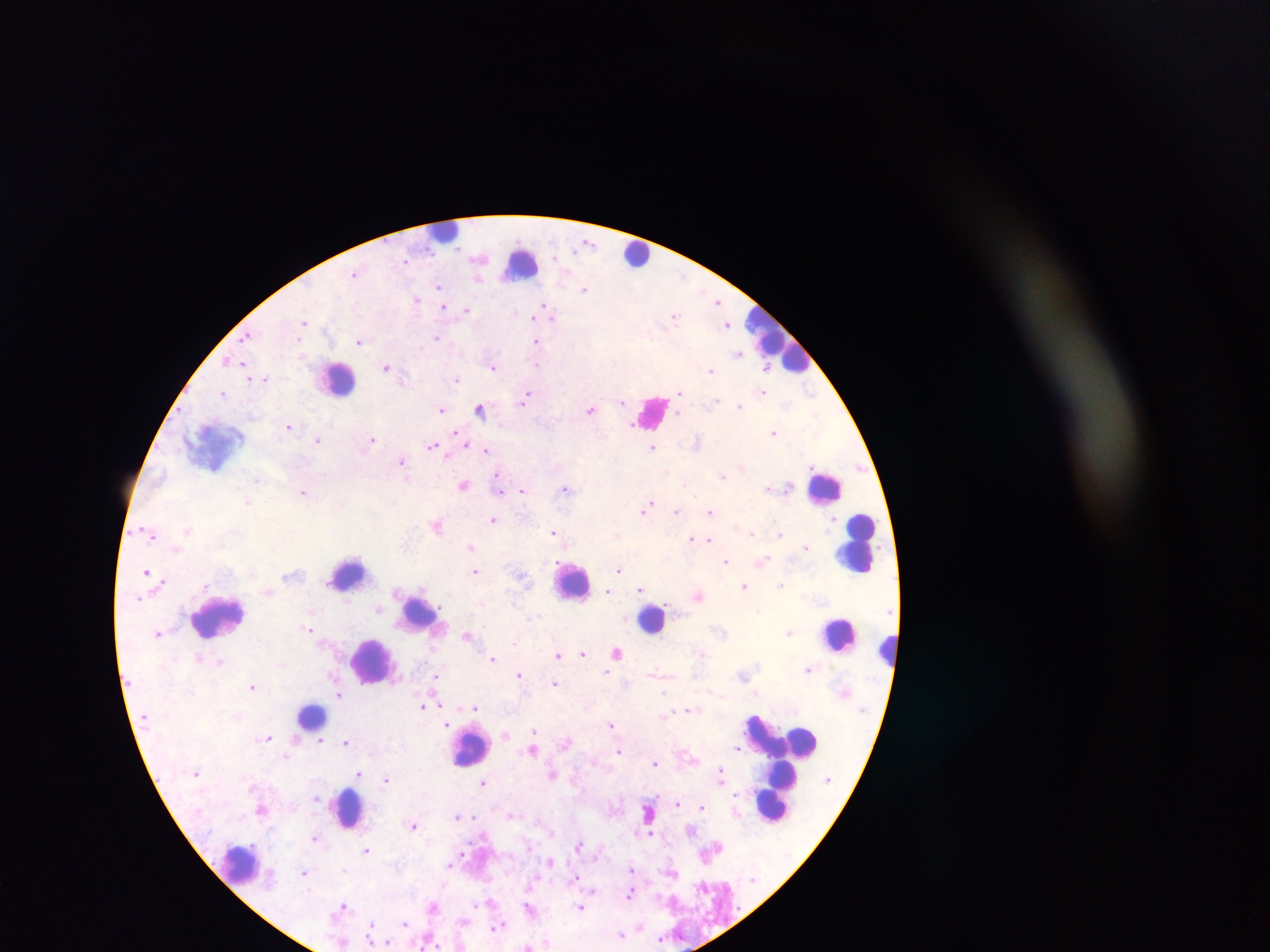

field of view = single
image size = 1270×952 pixels
leukocyte locations = approximate centers as [x, y] in pixels: [439, 233], [638, 256], [521, 260], [774, 343], [334, 378], [820, 486], [857, 547], [349, 573], [566, 584], [225, 610], [421, 611], [653, 618], [840, 636], [890, 648], [374, 662], [312, 719], [809, 737], [474, 743], [791, 773], [347, 806], [771, 806], [237, 862]
malaria parasite locations = approximate centers as [x, y] in pixels: [406, 257], [478, 258], [406, 259], [355, 273], [685, 274], [480, 278], [436, 289], [584, 289], [439, 291], [416, 298], [717, 302], [544, 306], [442, 307], [447, 308], [466, 310], [674, 314], [305, 320], [553, 320], [726, 324], [302, 326], [249, 335], [436, 338], [297, 342], [359, 342], [535, 342], [738, 354], [301, 356], [242, 362], [536, 366], [767, 366], [386, 367], [494, 368], [710, 369], [265, 376], [458, 379], [679, 390], [221, 392], [527, 392], [764, 392], [812, 393], [677, 395], [526, 397], [620, 401], [523, 403], [740, 406], [479, 407], [440, 408], [591, 410], [289, 425], [633, 426], [455, 431], [773, 432], [319, 439], [373, 440], [466, 443], [431, 446], [655, 449], [487, 450], [447, 459], [401, 462], [496, 473], [724, 476], [257, 480], [464, 486], [566, 488], [521, 490], [304, 492], [499, 493], [249, 503], [649, 503], [647, 509], [676, 511], [710, 512], [494, 519], [437, 526], [188, 530], [551, 532], [752, 533], [781, 533], [152, 535], [692, 538], [709, 539], [471, 547], [806, 547], [765, 560], [725, 562], [618, 570], [474, 571], [146, 573], [161, 582], [782, 584], [745, 587], [640, 591], [608, 592], [139, 600], [379, 609], [538, 616], [310, 629], [790, 632], [158, 633], [467, 637], [617, 652], [582, 654], [559, 655], [198, 658], [494, 658], [219, 662], [808, 669], [607, 672], [517, 674], [435, 675], [332, 676], [554, 683], [252, 687], [335, 689], [665, 692], [339, 694], [442, 707], [423, 708], [474, 708], [691, 708], [756, 713], [445, 720], [612, 724], [446, 725], [534, 732], [506, 734], [267, 737], [346, 741], [320, 742], [620, 749], [736, 749], [534, 751], [655, 763], [719, 769], [360, 772], [552, 775], [386, 779], [483, 783], [734, 793], [678, 803], [703, 805], [648, 811], [511, 815], [457, 817], [475, 817], [414, 826], [650, 832], [314, 837], [579, 842], [367, 850], [464, 851], [462, 857], [550, 862], [449, 867], [631, 868], [306, 873], [673, 874], [576, 876], [700, 885], [592, 893], [629, 895], [490, 901], [342, 905], [475, 905], [580, 907], [529, 911], [406, 922], [370, 923], [640, 924], [496, 927], [503, 927], [621, 933], [387, 939]
preparation = thick blood film
capture = mobile-phone photograph through a microscope
country = Ghana